Report the malaria status of this cell.
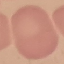

Uninfected.

Summary:
  - Preparation: thin smear
  - Image type: automatically extracted cell patch, resized to 64 × 64 pixels
  - Capture: smartphone camera at the microscope eyepiece
  - Stain: Giemsa